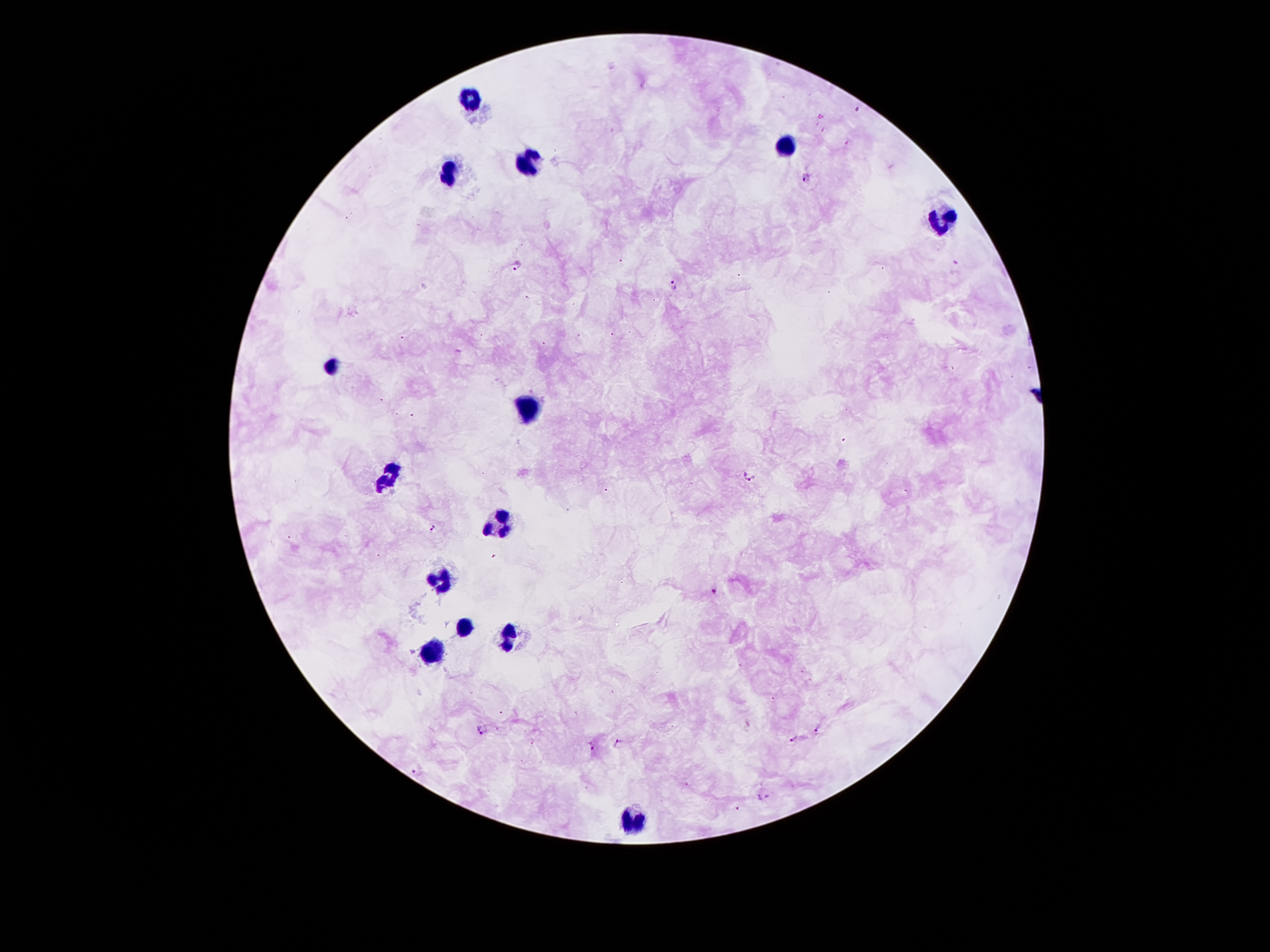

image_size: 1270×952 pixels
capture: smartphone camera through the microscope eyepiece
leukocyte_locations: 'approximate centers as {x, y} in pixels: {473, 98}, {785, 146}, {527, 163}, {447, 171}, {939, 223}, {332, 362}, {529, 410}, {386, 478}, {494, 524}, {441, 578}, {464, 626}, {510, 635}, {430, 653}, {630, 819}'
field_of_view: one from this slide
magnification: 100x
preparation: thick blood smear
malaria_parasite_locations: 'approximate centers as {x, y} in pixels: {803, 179}, {517, 267}, {674, 285}, {749, 474}, {434, 528}, {714, 591}, {818, 728}, {483, 730}, {794, 740}, {618, 743}, {591, 746}, {417, 771}, {765, 795}, {738, 807}'
stain: Giemsa
patient_malaria_status: positive for Plasmodium falciparum